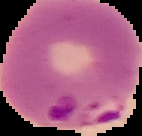
Summary:
  - Preparation: thin blood smear
  - Image size: 142×136 pixels
  - Malaria status: parasitized
  - Image type: segmented cell region on a black background